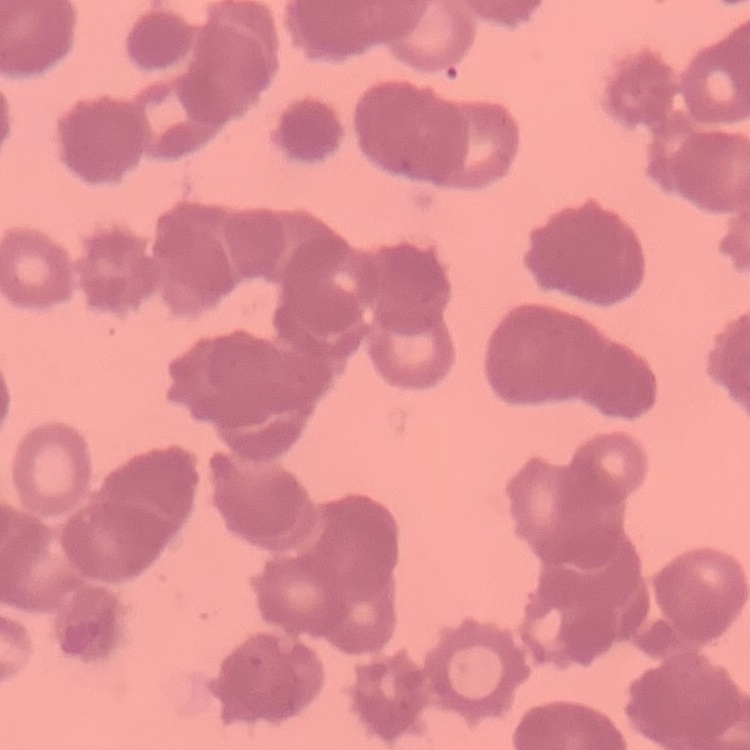

{
  "erythrocyte_morphology": "rouleaux formation",
  "stain": "Field's or Giemsa",
  "image_type": "one tile cut from a larger photomicrograph",
  "preparation": "thin blood smear"
}